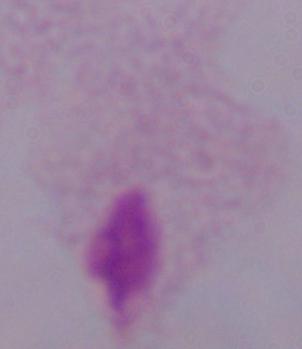

modality: micrograph
magnification: 1000x
identification: trichomonad